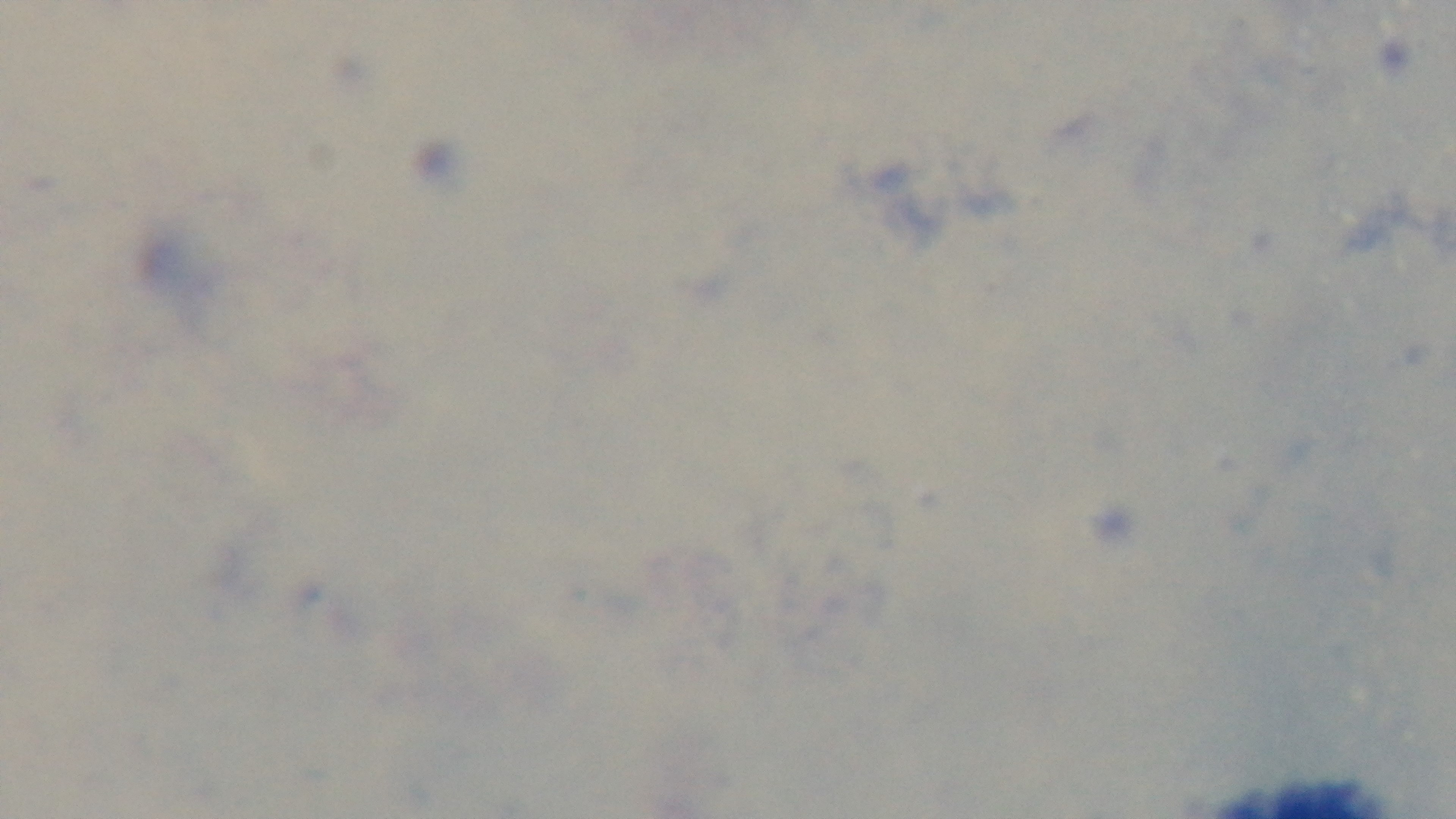

Summary:
  - Objective: 100x oil immersion
  - Malaria status: negative
  - Capture: mounted 4K digital camera
  - Stain: Giemsa
  - Modality: light microscopy
  - Preparation: thick smear
  - Field of view: one from the slide